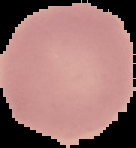

Summary:
  - Preparation: thin blood film
  - Image type: segmented cell region with the area outside set to black
  - Malaria status: uninfected
  - Image size: 136×148 pixels